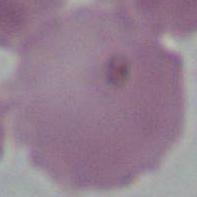

Summary:
  - Identification: red blood cell
  - Modality: photomicrograph
  - Magnification: 1000x